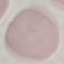

Summary:
  - Malaria status: uninfected
  - Stain: Giemsa
  - Preparation: thin smear
  - Capture: smartphone camera at the microscope eyepiece
  - Image type: cell patch, automatically extracted from a larger field of view and resized to 64 × 64 pixels